State which parasite is depicted.
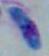

Toxoplasma gondii.

Micrograph. 1000x magnification.